Locate every blood parasite and identify its species.
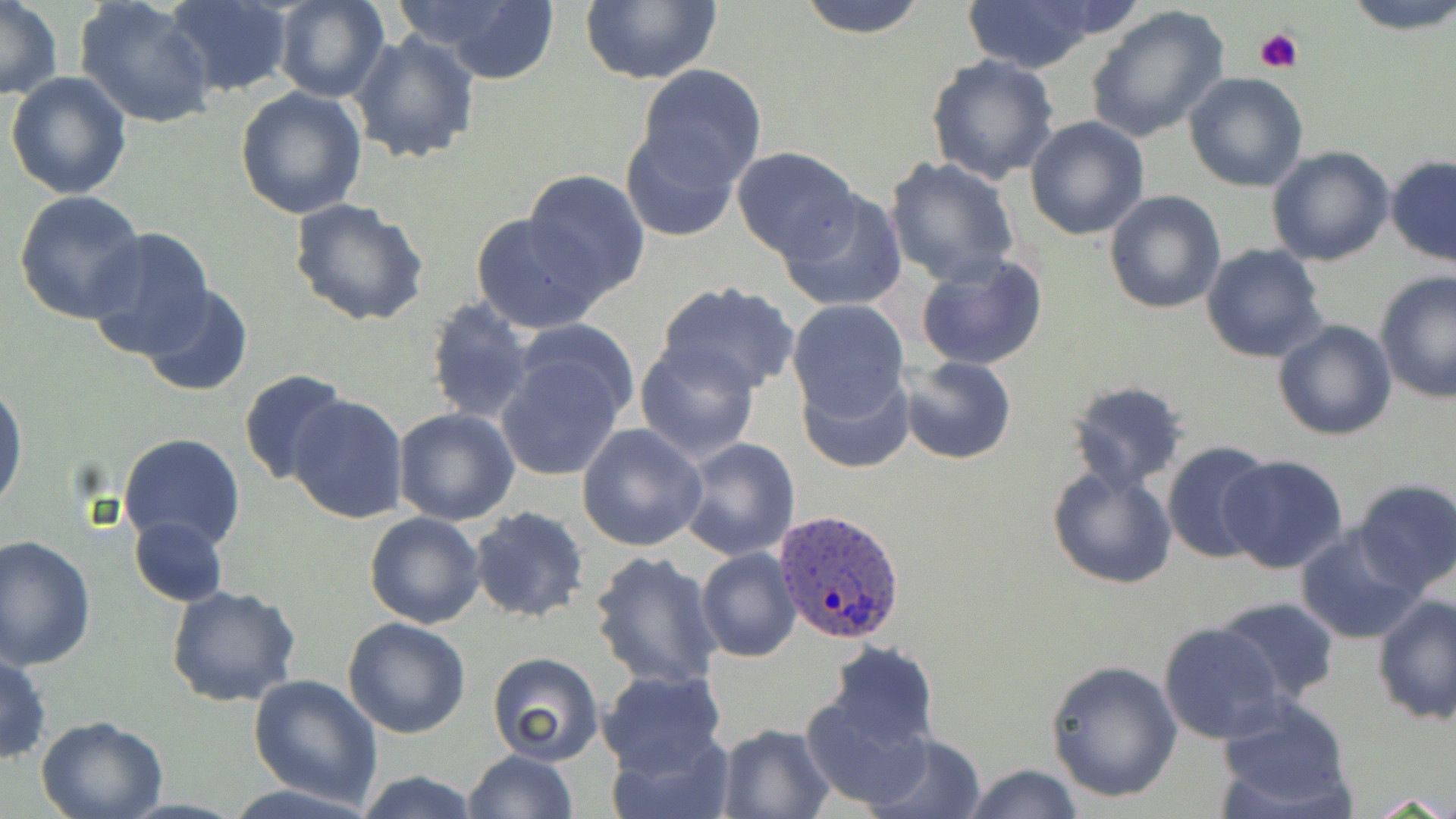

Approximate bounding boxes as [x1, y1, x2, y2] in pixels.
Plasmodium ovale-infected red blood cells: [773, 508, 907, 646].
No Plasmodium falciparum, Plasmodium malariae, Plasmodium vivax, Babesia divergens, or Trypanosoma brucei observed.

Platelet locations: [1254, 25, 1304, 75]. Uninfected red blood cell locations: [0, 0, 62, 102], [166, 0, 291, 97], [274, 0, 388, 104], [393, 0, 565, 80], [576, 0, 721, 86], [793, 0, 933, 38], [1343, 0, 1456, 36], [74, 1, 217, 129], [962, 1, 1105, 74], [1084, 4, 1231, 144], [351, 31, 481, 164], [925, 54, 1061, 186], [635, 64, 767, 188], [4, 71, 133, 198], [1183, 72, 1310, 191], [235, 85, 368, 219], [1025, 116, 1151, 240], [618, 122, 746, 243], [1266, 145, 1396, 266], [731, 147, 860, 263], [882, 156, 1022, 287], [1385, 156, 1456, 268], [522, 169, 653, 300], [776, 187, 910, 313], [1104, 189, 1226, 315], [13, 190, 149, 323], [288, 196, 432, 327], [470, 211, 606, 335], [83, 228, 216, 359], [1202, 244, 1328, 365], [914, 250, 1049, 371], [1374, 271, 1456, 405], [654, 282, 801, 397], [137, 286, 255, 399], [425, 295, 537, 426], [786, 299, 910, 422], [511, 318, 643, 425], [1272, 318, 1399, 441], [634, 339, 763, 463], [495, 352, 629, 482], [896, 355, 1018, 465], [797, 368, 913, 474], [238, 369, 355, 487], [1064, 380, 1190, 493], [0, 381, 27, 516], [286, 392, 413, 523], [393, 407, 520, 526], [576, 422, 709, 552], [117, 431, 247, 555], [676, 437, 801, 559], [1162, 440, 1276, 564], [1218, 453, 1349, 574], [1047, 463, 1179, 590], [1352, 478, 1456, 596], [470, 507, 591, 624], [364, 511, 486, 628], [128, 516, 228, 607], [1295, 525, 1426, 645], [0, 535, 96, 670], [697, 548, 803, 662], [589, 549, 724, 691], [165, 584, 301, 707], [1372, 594, 1456, 724], [1215, 596, 1340, 704], [342, 617, 471, 738], [1158, 622, 1287, 743], [820, 642, 939, 753], [0, 650, 50, 765], [484, 653, 605, 766], [1045, 659, 1184, 802], [598, 669, 729, 777], [247, 673, 381, 807], [800, 689, 934, 811], [1214, 696, 1355, 817], [34, 715, 168, 819], [715, 723, 837, 816], [608, 726, 735, 819], [864, 732, 987, 819], [462, 749, 579, 819], [961, 763, 1086, 819], [354, 770, 483, 819], [222, 782, 380, 819]. Slide-level diagnosis: Plasmodium ovale. Optical microscopy. Thin blood film. May-Grünwald-Giemsa stain. Captured at 1000x magnification. Image is 1456×819 pixels. One field of a larger specimen.